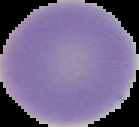

Summary:
  - Image type: segmented cell region with the area outside set to black
  - Preparation: thin blood film
  - Result: negative for malaria parasites
  - Image size: 139×127 pixels